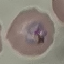 Result: malaria parasites identified. Giemsa stain. Cell patch, automatically extracted from a larger field of view and resized to 64 × 64 pixels. Thin blood film. Photographed with a smartphone camera at the microscope eyepiece.